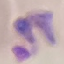
Result: malaria parasites identified. Giemsa stain. Thin smear of blood. Acquired by smartphone through the microscope eyepiece. Automatically extracted cell patch, resized to 64 × 64 pixels.